Assess the morphology of the red blood cells.
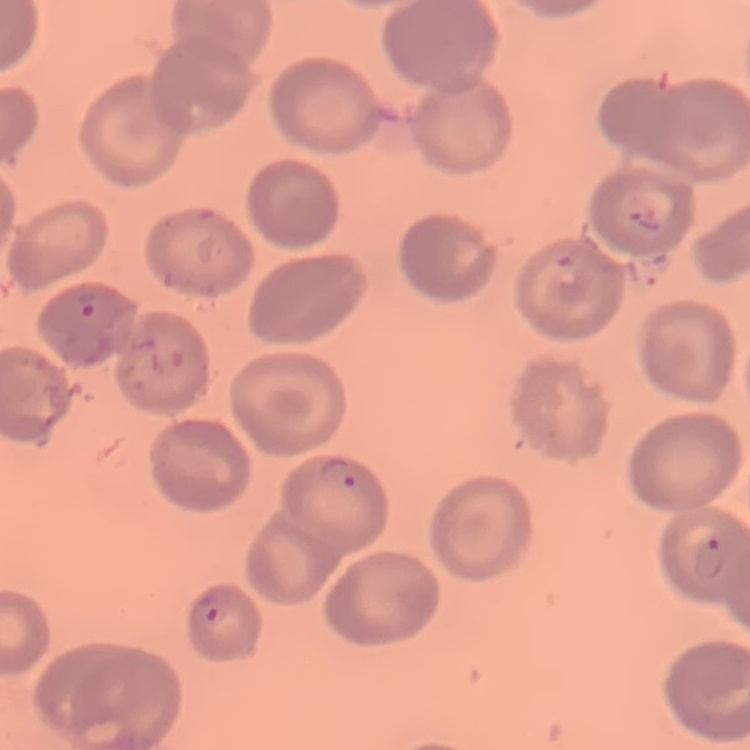

No rouleaux formation.

image type = square crop of a larger photomicrograph
stain = Field's or Giemsa
preparation = thin peripheral smear